Report the malaria status.
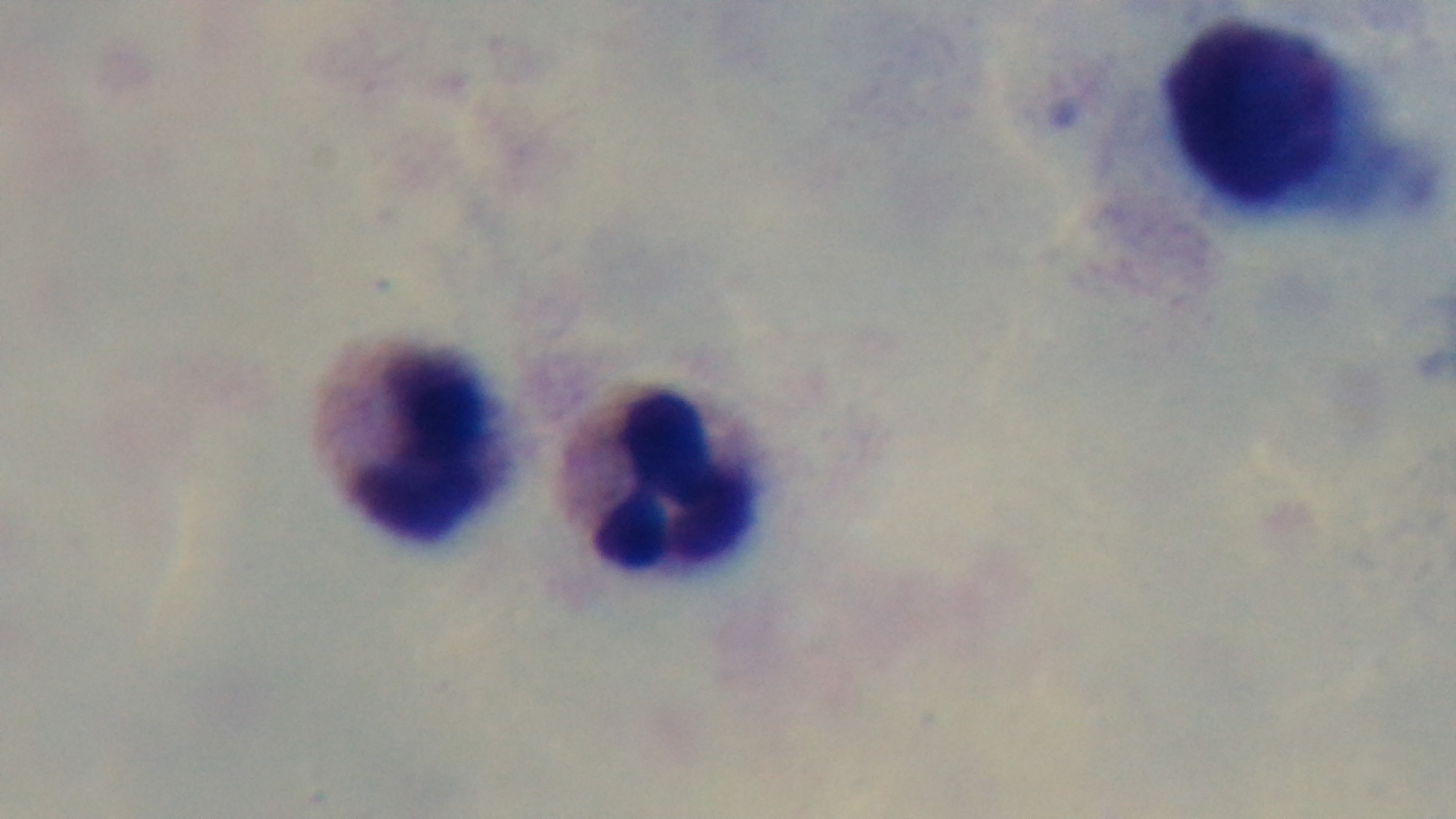
Uninfected.

Summary:
  - Preparation: thick smear
  - Modality: light microscopy
  - Objective: 100x oil immersion
  - Stain: Giemsa
  - Capture: mounted 4K digital camera
  - Field of view: one from the slide